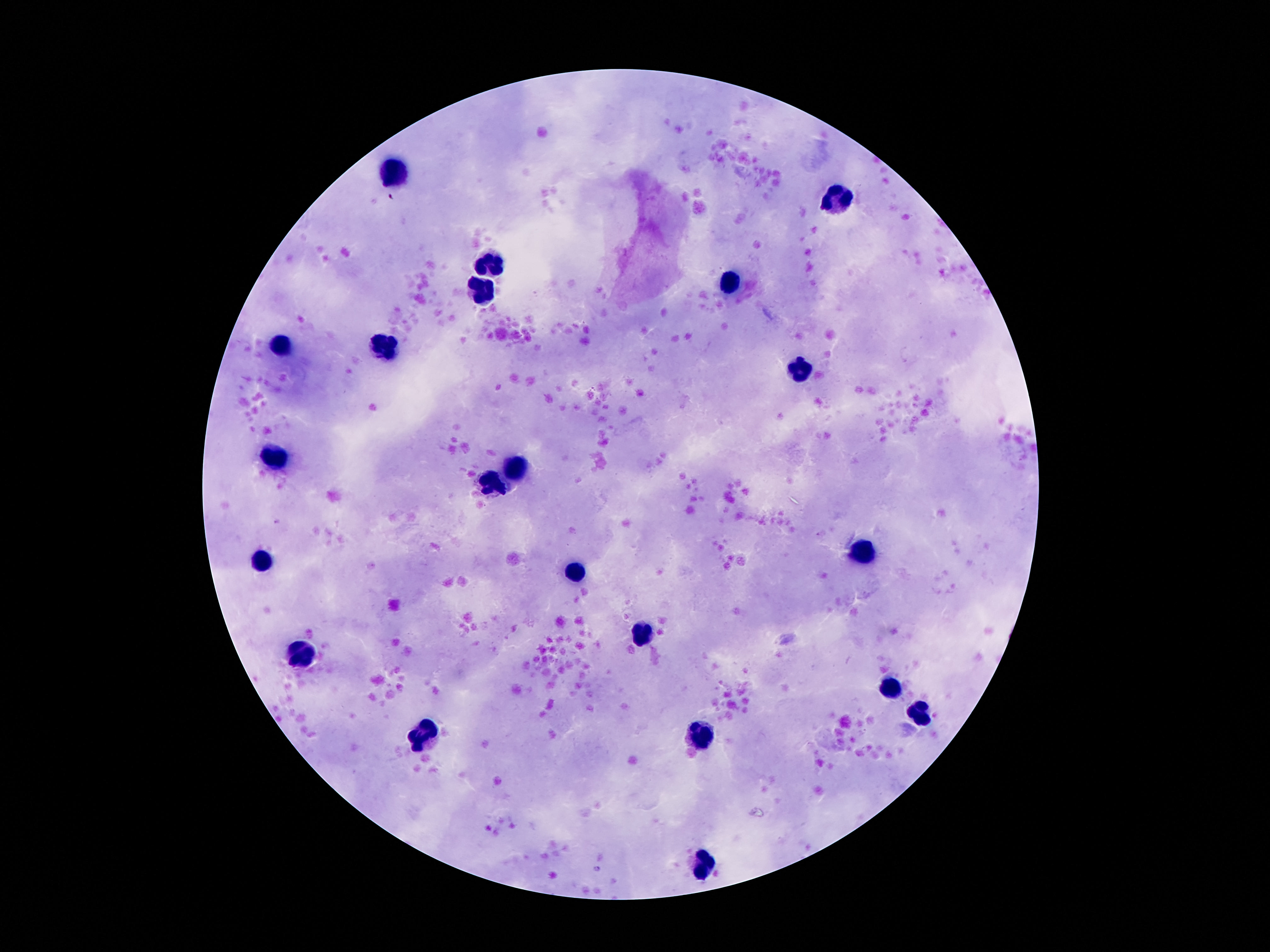
Approximate centers as {x, y} in pixels. Leukocyte locations: {395, 174}, {836, 200}, {493, 263}, {731, 282}, {483, 291}, {281, 343}, {383, 348}, {803, 370}, {274, 457}, {519, 462}, {493, 483}, {861, 551}, {260, 559}, {574, 572}, {644, 634}, {301, 654}, {890, 687}, {920, 713}, {423, 731}, {705, 738}, {703, 864}. 100x magnification. Smartphone photograph taken through the microscope eyepiece. Thick blood smear. Giemsa-stained preparation. Image is 1270×952 pixels. Patient malaria status: not infected. Single field of view.